Assess this cell for malaria.
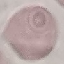

Uninfected.

Summary:
  - Stain: Giemsa
  - Capture: smartphone through the microscope eyepiece
  - Image type: cell patch, automatically extracted from a larger field of view and resized to 64 × 64 pixels
  - Preparation: thin smear